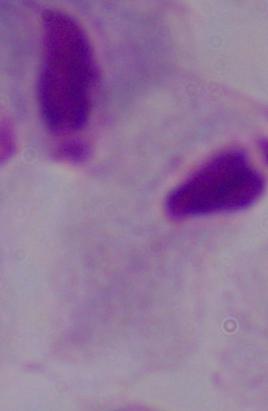
Summary:
  - Identification: trichomonad
  - Magnification: 1000x
  - Modality: photomicrograph